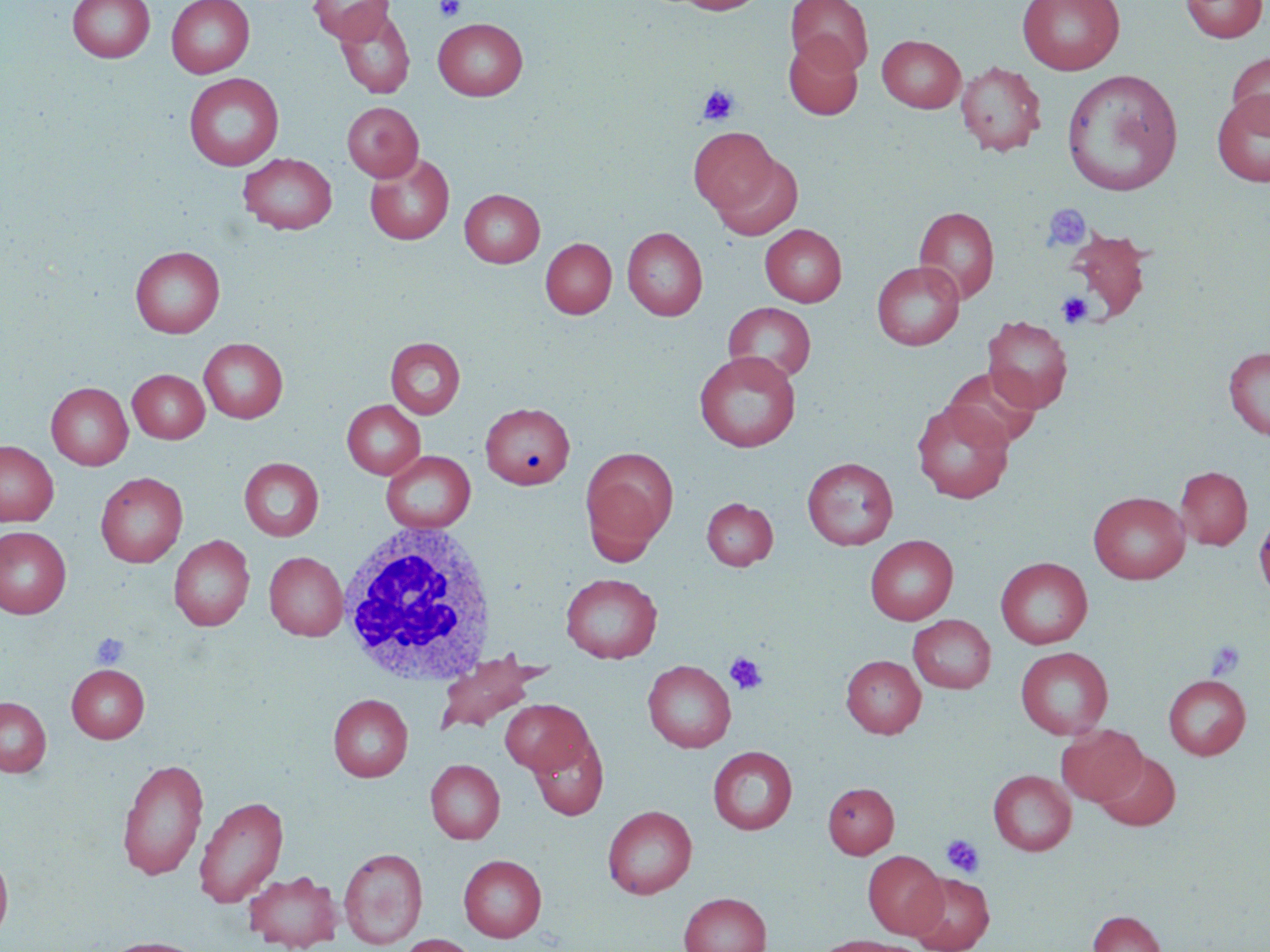
Summary:
  - Coordinate format: approximate bounding boxes as (x1, y1, x2, y2) in pixels
  - Platelet locations: (435, 0, 465, 21), (698, 84, 739, 125), (1042, 203, 1091, 252), (1057, 292, 1093, 328), (91, 633, 129, 668), (1206, 640, 1245, 680), (724, 653, 768, 695), (942, 835, 984, 878)
  - White blood cell locations: (335, 521, 498, 687)
  - Uninfected red blood cell locations: (67, 0, 155, 62), (166, 0, 254, 78), (308, 0, 394, 44), (671, 0, 765, 14), (786, 0, 873, 74), (1017, 0, 1124, 75), (1180, 0, 1267, 43), (334, 6, 415, 99), (433, 18, 528, 101), (784, 34, 863, 120), (877, 35, 965, 113), (1227, 51, 1270, 135), (956, 61, 1046, 156), (1061, 70, 1183, 197), (184, 73, 284, 171), (1212, 89, 1270, 187), (342, 102, 423, 181), (688, 126, 781, 217), (708, 151, 804, 240), (238, 153, 338, 234), (364, 153, 455, 245), (460, 189, 545, 267), (914, 206, 999, 303), (760, 224, 847, 307), (622, 227, 707, 320), (1065, 229, 1151, 322), (540, 237, 617, 319), (130, 246, 225, 337), (871, 261, 965, 350), (723, 302, 816, 384), (983, 316, 1073, 413), (386, 337, 465, 419), (199, 338, 288, 423), (1223, 347, 1270, 440), (694, 350, 801, 452), (943, 367, 1041, 451), (127, 369, 210, 443), (46, 382, 133, 470), (342, 400, 425, 479), (912, 400, 1014, 503), (481, 402, 575, 489), (0, 441, 58, 526), (581, 446, 678, 556), (381, 450, 476, 533), (803, 457, 898, 550), (239, 458, 324, 541), (1175, 466, 1252, 550), (95, 472, 188, 567), (1089, 491, 1189, 583), (702, 497, 778, 571), (1254, 513, 1270, 599), (0, 526, 72, 619), (168, 535, 255, 631), (865, 535, 958, 625), (264, 551, 348, 641), (996, 557, 1092, 648), (560, 573, 662, 663), (909, 615, 996, 693), (1015, 647, 1113, 739), (433, 654, 546, 737), (841, 655, 926, 738), (643, 660, 736, 752), (67, 664, 149, 743), (1164, 675, 1250, 759), (328, 694, 413, 782), (0, 696, 51, 776), (500, 699, 593, 775), (1057, 724, 1146, 806), (529, 733, 608, 820), (708, 746, 797, 834), (1095, 751, 1181, 831), (116, 757, 209, 882), (426, 759, 505, 844), (988, 769, 1076, 855), (823, 782, 899, 858), (193, 795, 288, 908), (602, 805, 697, 899), (339, 847, 428, 949), (0, 849, 14, 942), (863, 850, 947, 939), (458, 854, 547, 942), (243, 870, 342, 951), (908, 872, 995, 952), (679, 892, 771, 952), (1088, 910, 1166, 952), (396, 934, 480, 952), (814, 935, 918, 952), (99, 936, 210, 952)
  - Slide-level diagnosis: no evidence of blood parasites
  - Stain: May-Grünwald-Giemsa
  - Preparation: thin blood film
  - Image size: 1270×952 pixels
  - Field of view: one of a larger specimen
  - Modality: light microscopy
  - Magnification: 1000x